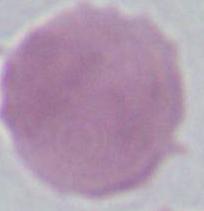
Photomicrograph. A red blood cell is seen. 1000x magnification.